Report the malaria status of this cell.
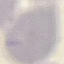
Uninfected.

Summary:
  - Preparation: thin blood film
  - Capture: smartphone through the microscope eyepiece
  - Stain: Giemsa
  - Image type: automatically extracted cell patch, resized to 64 × 64 pixels